Report the malaria status of this cell.
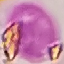
It is uninfected.

stain: Giemsa
preparation: thin blood smear
image_type: automatically extracted cell patch, resized to 64 × 64 pixels
capture: smartphone through the microscope eyepiece